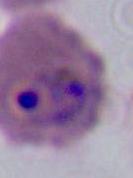

Captured at either 400x or 1000x magnification. Photomicrograph. A Plasmodium parasite is shown.